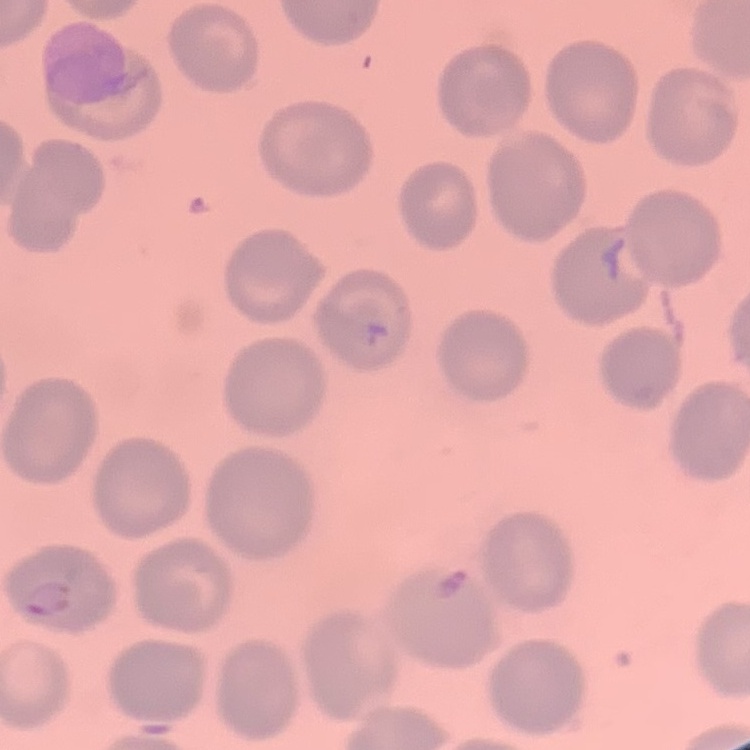
Summary:
  - Erythrocyte morphology: no rouleaux formation
  - Stain: Field's or Giemsa
  - Image type: one tile cut from a larger photomicrograph
  - Preparation: thin blood film